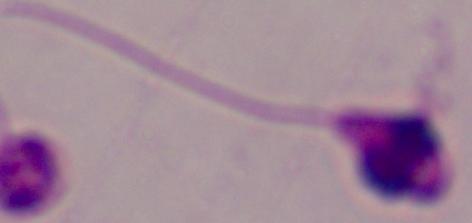

A Leishmania parasite is shown. Micrograph. 1000x magnification.